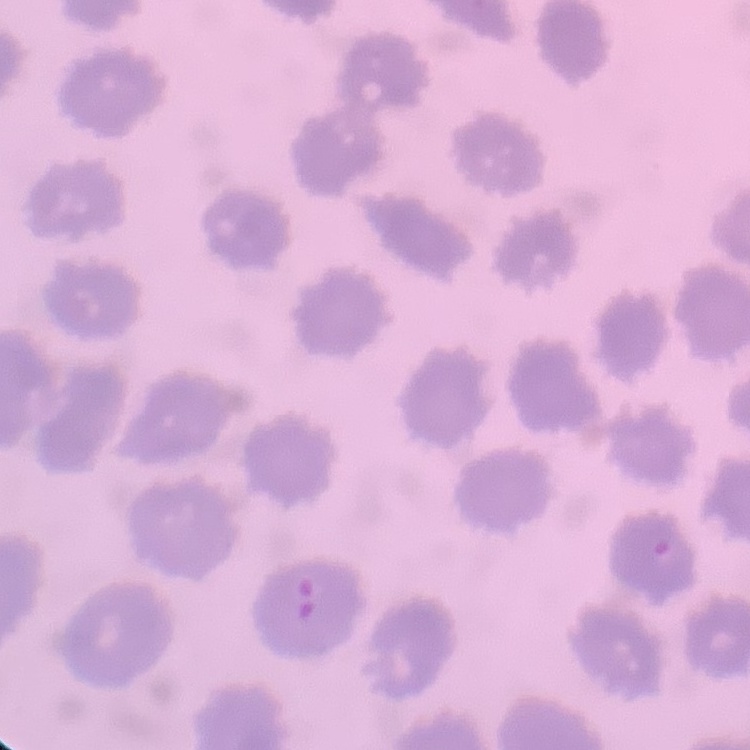
The erythrocytes show no rouleaux formation. Thin blood smear. Square crop of a larger photomicrograph. Stained with either Field's or Giemsa.